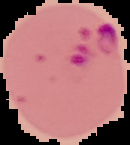
Summary:
  - Malaria status: parasitized
  - Image size: 130×145 pixels
  - Image type: cell region segmented out of the field of view; surrounding area masked to black
  - Preparation: thin blood smear